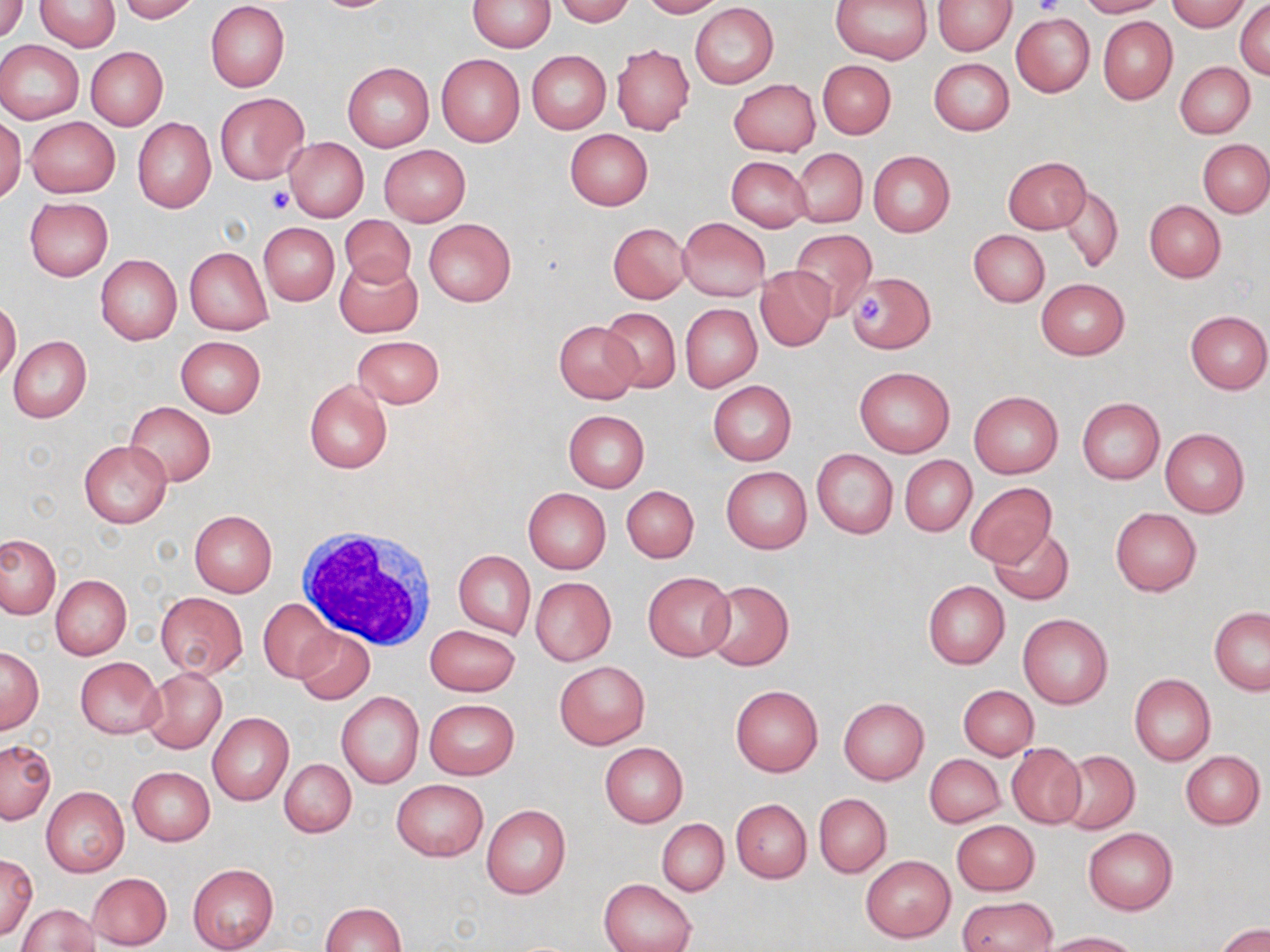

Approximate bounding boxes as [x1, y1, x2, y2] in pixels. White blood cell locations: [298, 524, 440, 649]. Uninfected red blood cell locations: [2, 0, 29, 40], [119, 0, 201, 23], [467, 0, 557, 52], [552, 0, 634, 25], [639, 0, 722, 18], [831, 0, 934, 65], [934, 0, 1016, 55], [1075, 0, 1164, 17], [1168, 0, 1249, 31], [34, 1, 120, 51], [1235, 1, 1270, 79], [206, 2, 290, 93], [690, 3, 778, 88], [1010, 12, 1095, 97], [1098, 16, 1177, 104], [0, 40, 84, 123], [612, 45, 695, 136], [85, 47, 168, 130], [526, 50, 611, 133], [435, 52, 524, 147], [929, 57, 1014, 135], [818, 60, 896, 140], [342, 61, 434, 151], [1175, 61, 1255, 137], [728, 78, 821, 156], [215, 92, 309, 184], [0, 116, 25, 203], [25, 117, 120, 197], [132, 117, 217, 213], [564, 128, 653, 210], [285, 137, 368, 222], [1199, 141, 1270, 217], [378, 145, 470, 226], [793, 149, 866, 226], [868, 151, 955, 236], [726, 155, 812, 231], [1003, 156, 1091, 234], [1060, 184, 1123, 272], [24, 198, 113, 281], [1144, 201, 1226, 283], [339, 215, 417, 289], [678, 217, 770, 300], [424, 218, 517, 306], [258, 223, 339, 306], [608, 223, 691, 303], [789, 228, 877, 318], [969, 229, 1049, 307], [184, 246, 273, 335], [96, 255, 182, 345], [335, 257, 423, 338], [756, 266, 835, 350], [846, 270, 935, 352], [1035, 279, 1128, 360], [0, 299, 20, 383], [680, 303, 762, 391], [599, 307, 682, 392], [1185, 310, 1270, 393], [553, 321, 640, 404], [352, 335, 444, 408], [8, 336, 92, 422], [175, 336, 266, 417], [854, 367, 955, 456], [305, 379, 393, 473], [708, 381, 796, 465], [969, 391, 1063, 478], [1077, 398, 1164, 484], [124, 402, 217, 485], [563, 409, 649, 492], [88, 414, 206, 512], [1159, 429, 1249, 517], [79, 440, 171, 529], [813, 450, 897, 538], [900, 455, 976, 536], [721, 466, 811, 554], [965, 482, 1057, 567], [621, 485, 699, 564], [523, 488, 611, 573], [1110, 507, 1202, 596], [190, 510, 277, 597], [989, 526, 1074, 605], [0, 535, 60, 618], [454, 549, 535, 640], [643, 572, 735, 662], [52, 575, 131, 659], [530, 577, 615, 665], [703, 580, 793, 671], [922, 581, 1009, 669], [155, 591, 248, 678], [259, 597, 338, 683], [1209, 607, 1269, 694], [1018, 614, 1114, 709], [426, 624, 520, 696], [295, 626, 374, 703], [0, 648, 43, 732], [75, 658, 164, 737], [554, 660, 650, 749], [142, 667, 227, 754], [1129, 674, 1216, 765], [730, 684, 823, 775], [957, 685, 1038, 760], [336, 691, 424, 789], [839, 697, 929, 784], [425, 699, 519, 780], [207, 712, 293, 805], [0, 740, 56, 824], [599, 742, 687, 827], [1006, 744, 1086, 828], [1057, 750, 1139, 833], [1180, 750, 1266, 829], [925, 754, 1004, 827], [280, 759, 357, 837], [127, 766, 215, 845], [392, 779, 488, 861], [42, 786, 128, 877], [814, 793, 891, 877], [731, 799, 811, 883], [482, 805, 571, 900], [657, 818, 728, 896], [951, 819, 1039, 895], [1084, 828, 1177, 914], [1, 854, 37, 941], [861, 855, 955, 943], [187, 864, 279, 952], [87, 872, 172, 950], [0, 875, 73, 946], [599, 879, 695, 952], [958, 896, 1057, 952], [18, 902, 99, 952], [319, 902, 406, 952], [1217, 923, 1269, 952], [1038, 931, 1139, 951]. Platelet locations: [1033, 0, 1064, 17], [266, 188, 294, 214], [859, 296, 882, 323]. Slide-level diagnosis: no evidence of blood parasites. One field of a larger specimen. Captured at 1000x magnification. Light microscopy. May-Grünwald-Giemsa stain. Image is 1270×952 pixels. Thin blood film.